Outline platelets.
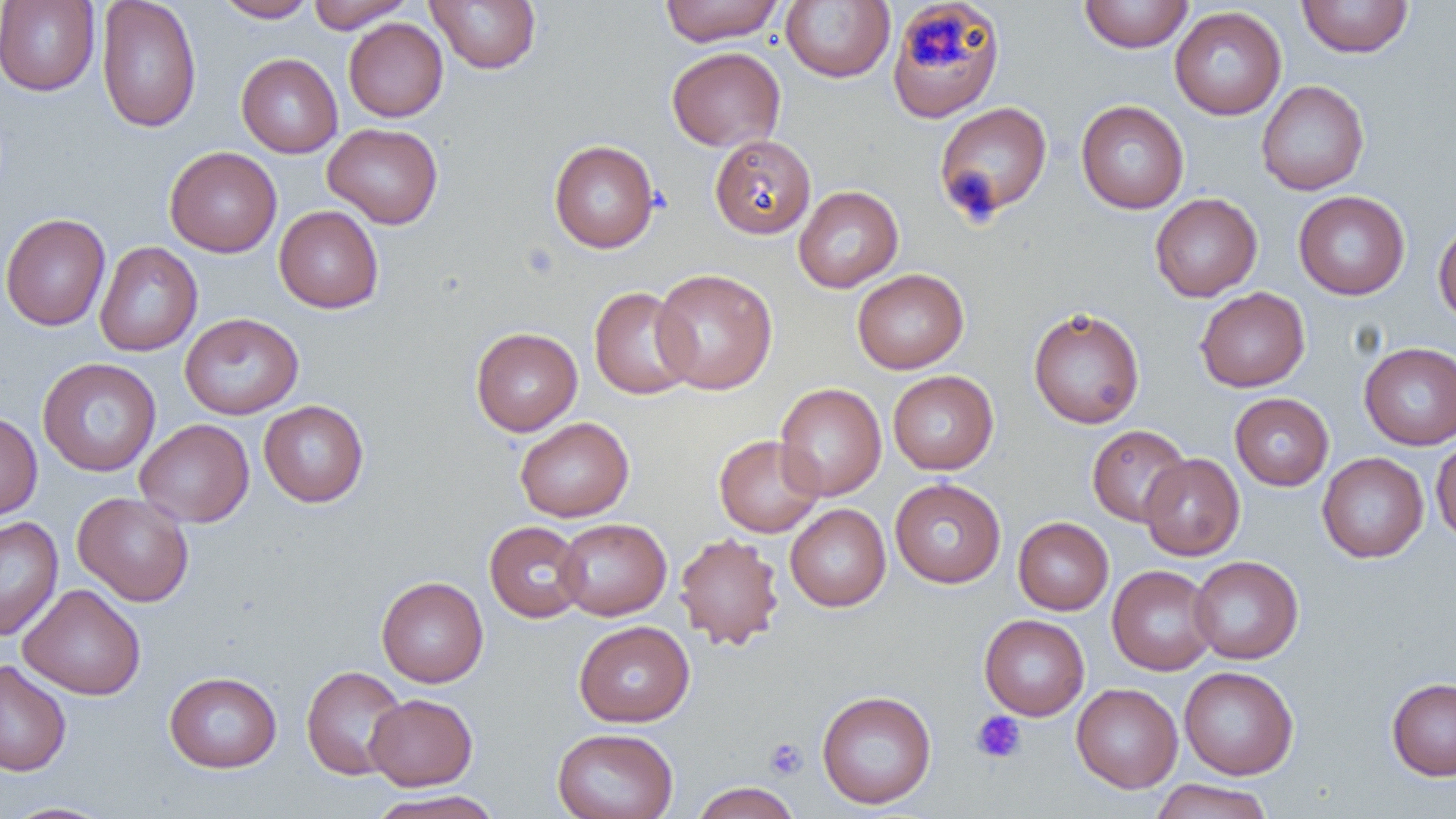
Approximate bounding boxes as (x1,y1)-(x2,y2) corner pairs in pixels.
Platelets: (907,19)-(963,66), (972,710)-(1027,764), (764,737)-(808,779).

Summary:
  - Uninfected red blood cell locations: (96,0)-(201,134), (213,0)-(317,22), (305,0)-(415,32), (426,0)-(542,73), (659,0)-(786,45), (1078,0)-(1194,53), (1297,0)-(1414,58), (0,1)-(100,96), (780,1)-(895,83), (888,2)-(1005,122), (1169,6)-(1286,120), (343,18)-(448,122), (667,47)-(785,151), (236,53)-(343,158), (1256,80)-(1369,195), (1076,100)-(1189,214), (933,101)-(1053,222), (323,123)-(443,229), (709,135)-(816,239), (548,139)-(660,253), (165,147)-(282,257), (793,185)-(903,292), (1293,190)-(1410,300), (1150,193)-(1262,302), (274,205)-(384,313), (0,213)-(111,331), (1433,220)-(1456,325), (94,241)-(203,357), (651,268)-(778,395), (852,269)-(968,374), (588,286)-(699,399), (1195,287)-(1309,392), (1028,307)-(1145,429), (179,313)-(304,419), (471,327)-(583,436), (1359,342)-(1456,450), (37,357)-(161,477), (888,371)-(998,475), (775,383)-(887,501), (1230,392)-(1334,491), (258,400)-(369,507), (0,411)-(42,521), (515,417)-(634,522), (135,418)-(254,527), (1087,424)-(1192,526), (713,434)-(824,538), (1431,436)-(1456,543), (1317,453)-(1429,563), (1139,454)-(1245,561), (890,478)-(1006,588), (72,491)-(194,606), (785,504)-(891,611), (0,516)-(63,641), (1013,517)-(1113,615), (556,518)-(671,620), (484,521)-(588,623), (674,532)-(785,650), (1189,555)-(1304,664), (1107,565)-(1218,675), (376,576)-(489,687), (18,583)-(145,700), (979,614)-(1089,720), (573,620)-(695,727), (0,660)-(72,776), (301,665)-(408,780), (1179,666)-(1298,780), (164,671)-(282,773), (1387,677)-(1456,780), (1071,683)-(1183,793), (816,689)-(937,809), (365,693)-(478,790), (551,728)-(678,819), (1150,779)-(1274,819), (690,782)-(801,819), (366,790)-(503,819), (2,801)-(117,819)
  - Slide-level diagnosis: negative for blood parasites
  - Image size: 1456×819 pixels
  - Preparation: thin blood film
  - Field of view: one of a larger specimen
  - Magnification: 1000x
  - Modality: light microscopy